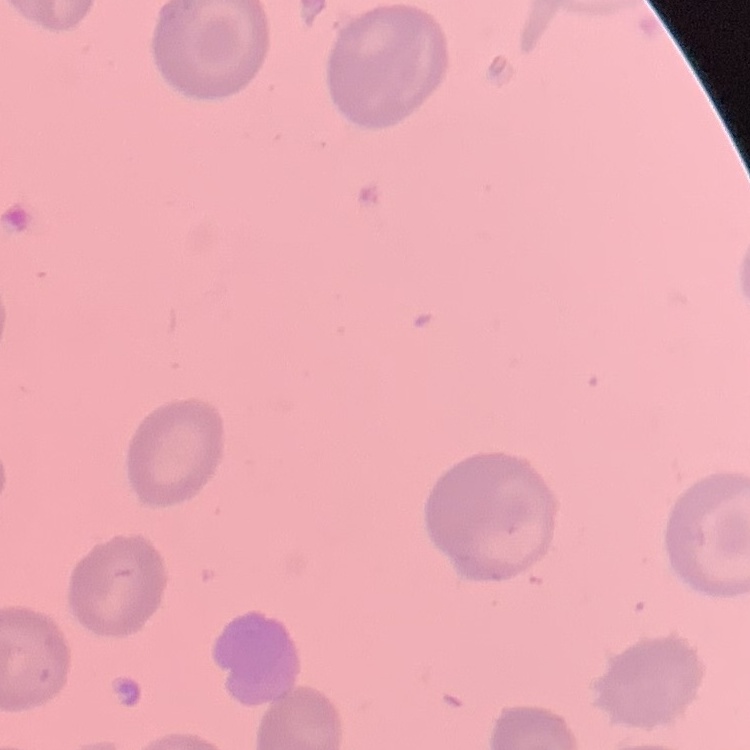

erythrocyte_morphology: no rouleaux formation
preparation: thin blood smear
stain: Field's or Giemsa
image_type: one tile cut from a larger photomicrograph